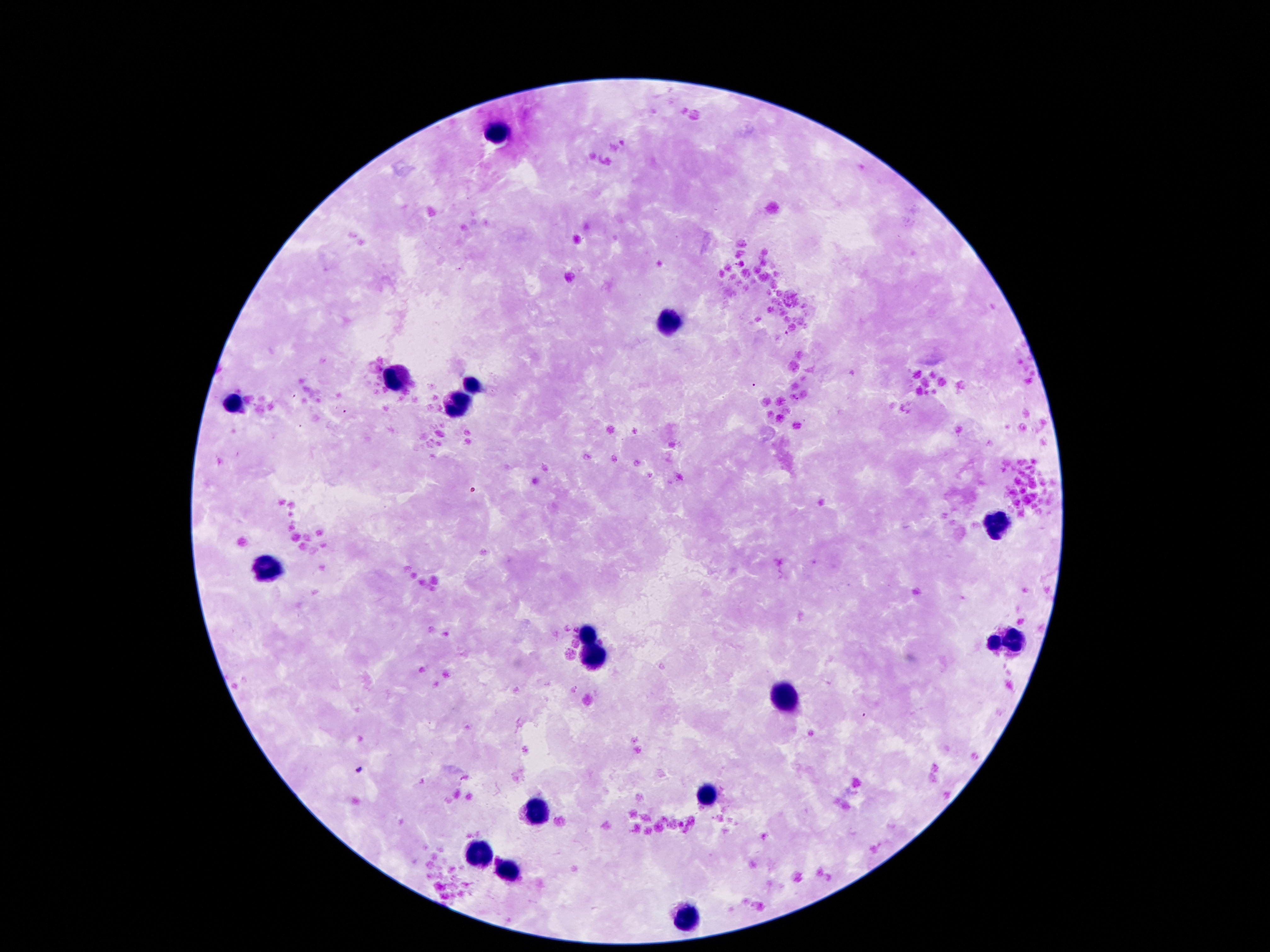

stain = Giemsa
image size = 1270×952 pixels
capture = smartphone camera through the microscope eyepiece
patient malaria status = uninfected
magnification = 100x
leukocyte locations = approximate centers as {x, y} in pixels: {495, 136}, {665, 325}, {395, 376}, {470, 383}, {459, 407}, {994, 518}, {265, 567}, {590, 637}, {1019, 643}, {992, 646}, {594, 661}, {780, 699}, {705, 794}, {539, 807}, {481, 854}, {510, 872}, {685, 922}
preparation = thick blood film
field of view = single